Report the malaria status of this cell.
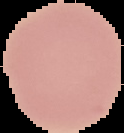

Uninfected.

Segmented cell region on a black background. From a thin blood smear. Image is 124×133 pixels.